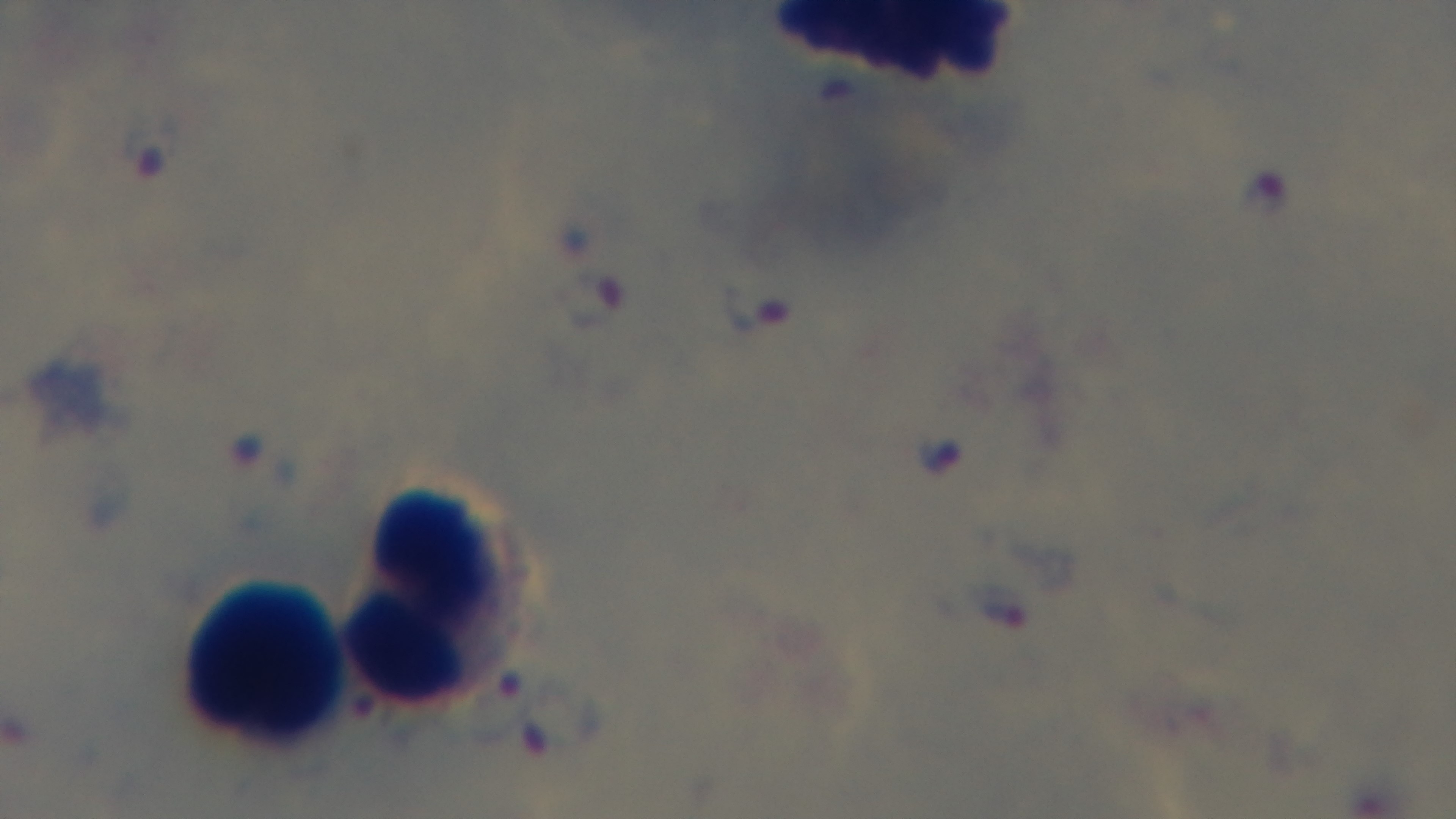 Malaria status: infected. Light microscopy. Mounted 4K digital camera. Oil-immersion objective, 100x. Giemsa-stained. Preparation: thick blood film. One field from the slide.